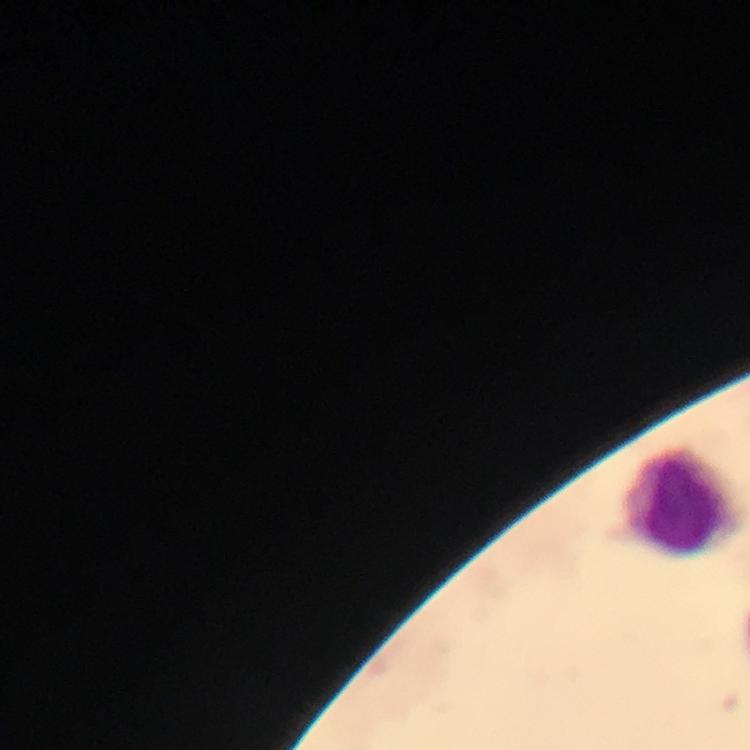

Approximate centers as [x, y] in pixels.
Summary:
  - Leukocyte locations: [685, 502]
  - Malaria parasites: none seen
  - Capture: smartphone camera through the microscope
  - Context: from a diagnostic examination for malaria
  - Preparation: thick smear
  - Magnification: 100x
  - Cropped from: one field of view
  - Stain: Giemsa
  - Image size: 750×750 pixels
  - Immersion oil: applied